Locate every Plasmodium parasite.
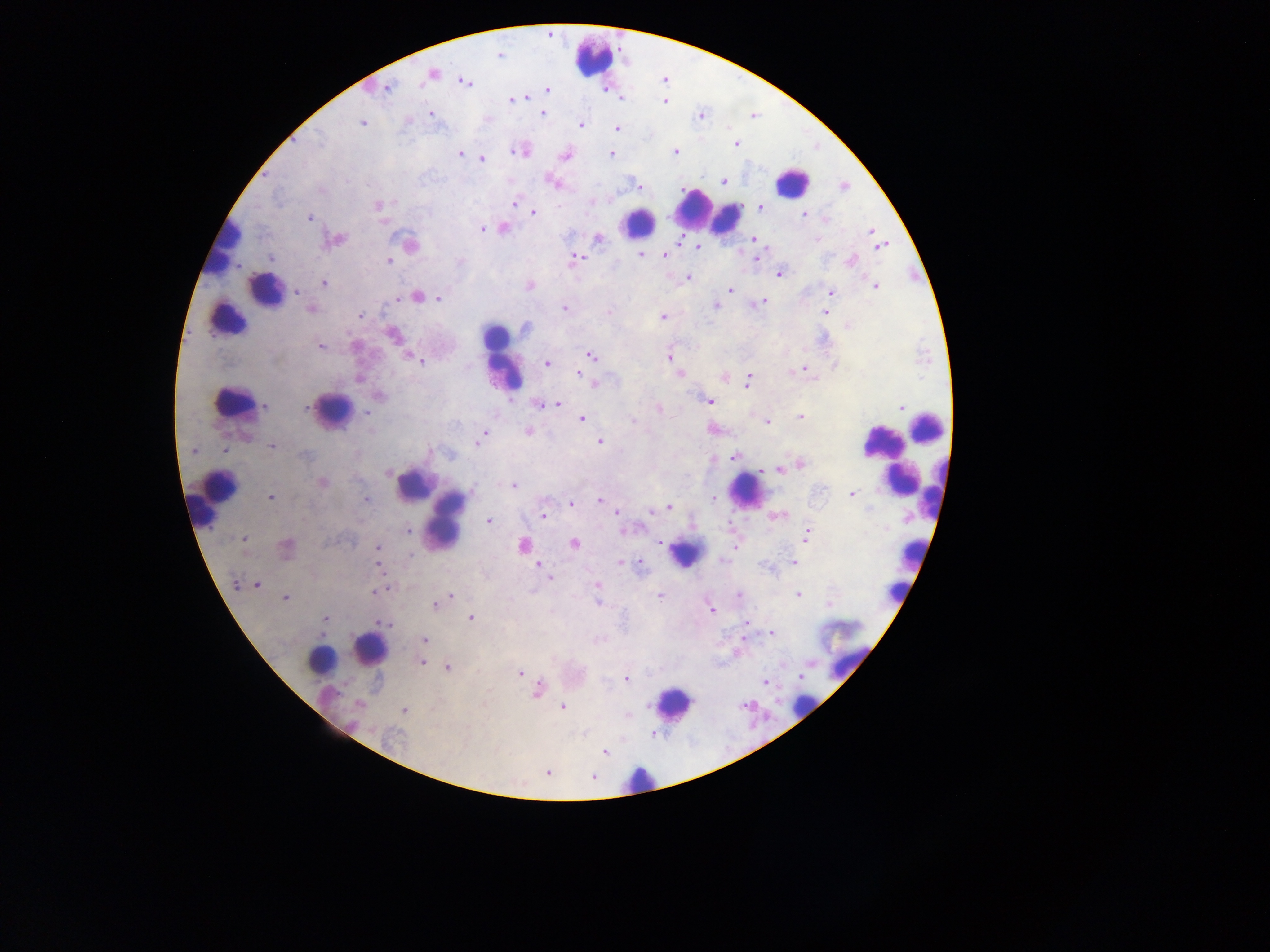
Approximate centers as (x, y) in pixels.
Plasmodium parasites: (499, 55), (432, 73), (464, 82), (387, 88), (548, 90), (527, 98), (512, 100), (664, 101), (431, 114), (543, 114), (700, 116), (407, 122), (362, 123), (581, 126), (617, 128), (319, 139), (736, 144), (520, 151), (512, 152), (675, 152), (461, 154), (611, 154), (566, 156), (482, 159), (724, 181), (552, 182), (638, 186), (845, 187), (321, 191), (514, 204), (377, 206), (760, 209), (533, 213), (804, 215), (309, 218), (824, 218), (482, 229), (503, 229), (871, 231), (339, 239), (598, 239), (753, 239), (816, 239), (679, 241), (411, 245), (880, 246), (698, 248), (640, 255), (665, 256), (757, 256), (271, 258), (576, 258), (389, 260), (851, 261), (780, 274), (689, 277), (323, 284), (529, 286), (875, 287), (730, 290), (297, 292), (830, 292), (417, 296), (439, 299), (398, 300), (761, 302), (752, 305), (716, 307), (564, 308), (310, 309), (608, 312), (825, 312), (360, 316), (663, 317), (847, 326), (527, 327), (392, 334), (321, 348), (591, 355), (409, 357), (668, 358), (421, 362), (546, 363), (835, 365), (804, 369), (792, 372), (579, 374), (680, 374), (358, 380), (747, 382), (594, 383), (380, 396), (710, 401), (558, 404), (540, 405), (265, 406), (900, 406), (306, 408), (659, 409), (367, 413), (801, 417), (582, 419), (633, 421), (766, 421), (528, 432), (485, 434), (479, 440), (600, 442), (476, 443), (272, 446), (223, 450), (193, 451), (304, 455), (733, 457), (800, 464), (778, 469), (389, 473), (323, 483), (513, 485), (851, 493), (271, 497), (713, 498), (367, 500), (600, 500), (571, 504), (669, 507), (617, 513), (542, 515), (777, 516), (489, 521), (407, 531), (807, 535), (244, 539), (660, 543), (574, 544), (522, 546), (286, 547), (734, 547), (378, 548), (412, 555), (722, 560), (794, 562), (622, 563), (538, 565), (378, 566), (640, 566), (546, 574), (549, 578), (237, 585), (257, 585), (597, 585), (377, 592), (738, 594), (798, 594), (450, 596), (658, 596), (285, 598), (598, 602), (435, 604), (711, 609), (470, 618), (326, 619), (746, 623), (383, 624), (772, 633), (425, 640), (421, 662), (447, 667), (519, 673), (627, 679), (765, 682), (538, 690), (358, 705), (562, 707), (404, 711), (628, 714), (604, 752), (548, 772), (592, 777).

Leukocyte locations: (595, 59), (792, 182), (705, 209), (724, 218), (639, 221), (224, 245), (267, 288), (226, 317), (495, 338), (503, 360), (233, 402), (332, 409), (927, 426), (882, 441), (891, 464), (899, 477), (413, 486), (745, 490), (939, 494), (217, 498), (447, 519), (686, 554), (912, 555), (895, 591), (837, 632), (370, 650), (319, 660), (849, 661), (673, 703), (803, 706), (639, 779). Mobile-phone photograph taken through the microscope. Thick blood smear. Collected in Ghana. Single field of view. Image is 1270×952 pixels.